Identify the parasite.
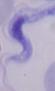

This is a trypanosome.

magnification = 1000x
modality = photomicrograph